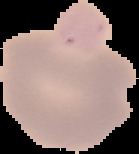

preparation: thin blood smear
image_type: segmented cell region on a black background
image_size: 139×154 pixels
result: negative for malaria parasites